State which parasite is depicted.
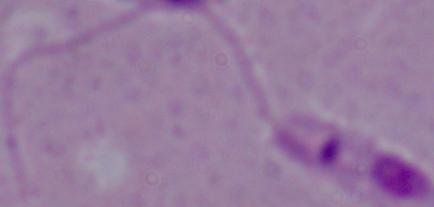
Leishmania.

{
  "magnification": "1000x",
  "modality": "micrograph"
}